Describe the morphology of the red blood cells.
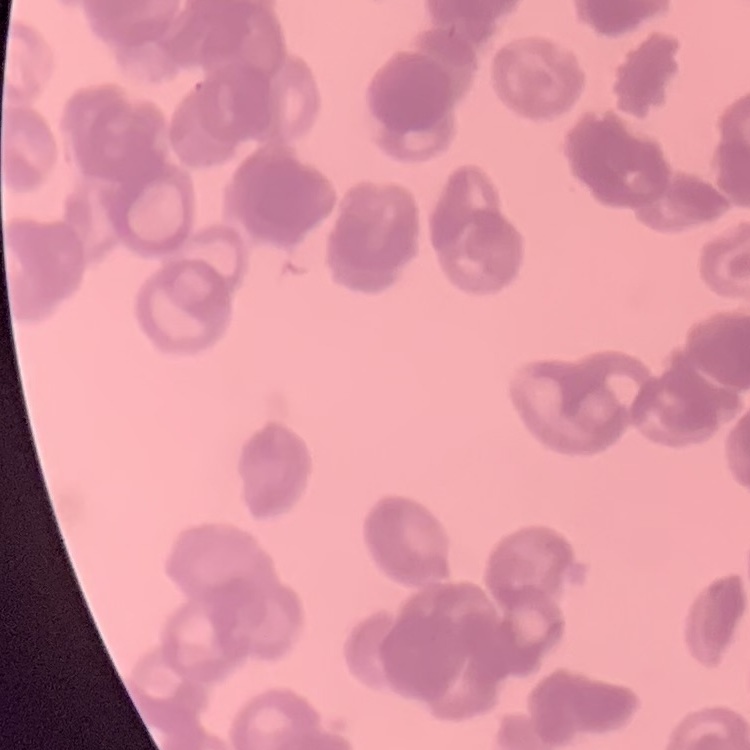

Rouleaux formation.

One tile cut from a larger photomicrograph. Stained with either Field's or Giemsa. Thin peripheral smear.